Assess the morphology of the erythrocytes.
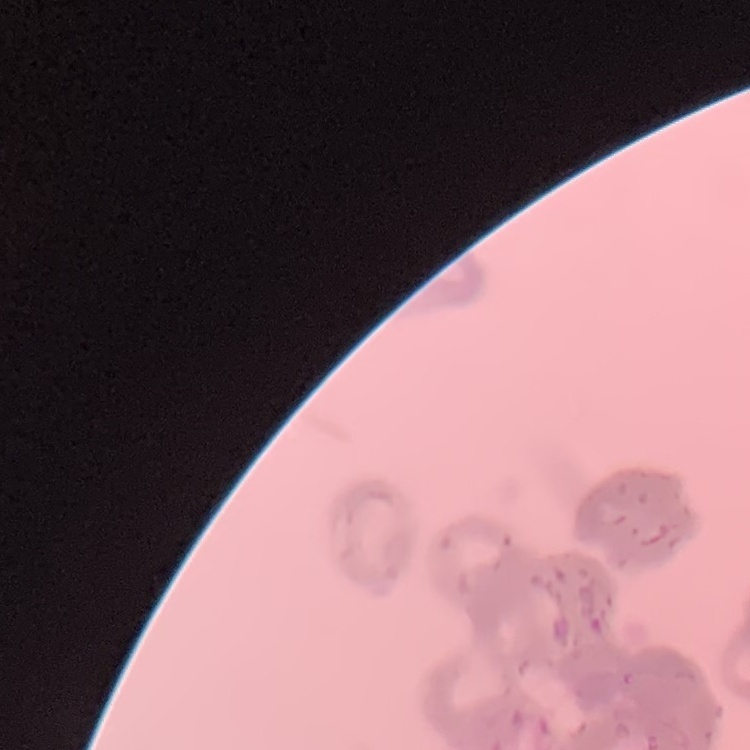
Rouleaux formation.

Summary:
  - Preparation: thin peripheral smear
  - Image type: one tile cut from a larger photomicrograph
  - Stain: Field's or Giemsa